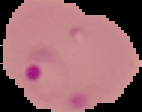

image size = 142×112 pixels
image type = segmented cell region with the area outside set to black
malaria status = parasitized
preparation = thin blood film